Outline each blood parasite and name the species.
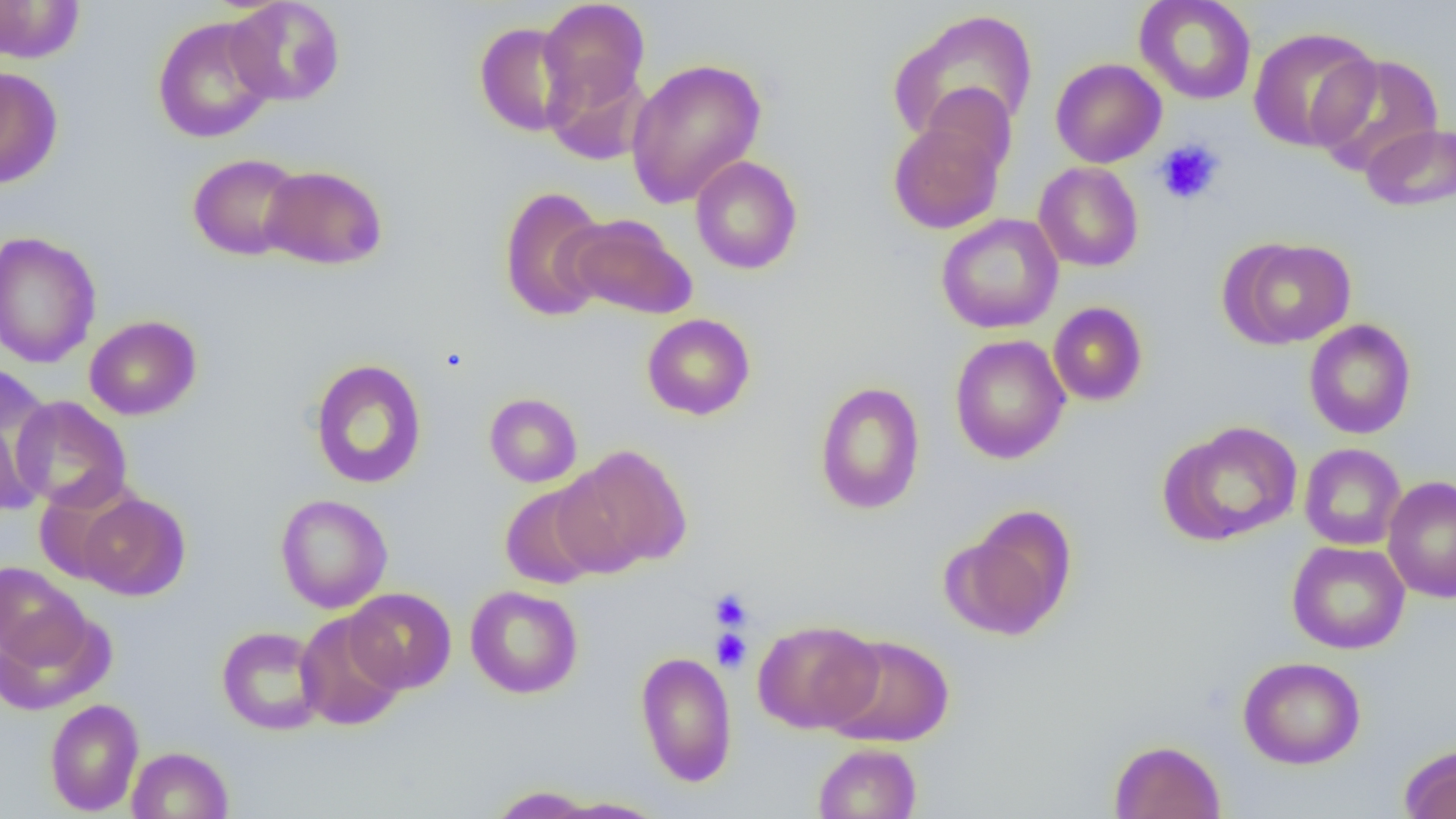
No blood parasites seen.

Approximate bounding boxes as named x1/y1/x2/y2 corners in pixels. Uninfected red blood cell locations: (x1=226, y1=0, x2=346, y2=106), (x1=1134, y1=0, x2=1257, y2=105), (x1=0, y1=1, x2=84, y2=63), (x1=538, y1=1, x2=650, y2=109), (x1=888, y1=8, x2=1038, y2=145), (x1=152, y1=15, x2=277, y2=144), (x1=474, y1=22, x2=579, y2=137), (x1=1248, y1=26, x2=1380, y2=152), (x1=1310, y1=52, x2=1445, y2=177), (x1=625, y1=58, x2=767, y2=208), (x1=1050, y1=58, x2=1166, y2=168), (x1=543, y1=59, x2=652, y2=166), (x1=0, y1=66, x2=63, y2=189), (x1=919, y1=83, x2=1018, y2=180), (x1=888, y1=119, x2=1005, y2=234), (x1=1361, y1=123, x2=1456, y2=211), (x1=187, y1=153, x2=305, y2=261), (x1=689, y1=155, x2=802, y2=275), (x1=1033, y1=161, x2=1144, y2=272), (x1=260, y1=164, x2=388, y2=270), (x1=498, y1=186, x2=612, y2=323), (x1=564, y1=213, x2=698, y2=320), (x1=936, y1=213, x2=1064, y2=334), (x1=0, y1=230, x2=102, y2=369), (x1=1221, y1=236, x2=1357, y2=349), (x1=1048, y1=302, x2=1148, y2=406), (x1=642, y1=313, x2=755, y2=420), (x1=84, y1=315, x2=201, y2=420), (x1=1303, y1=319, x2=1416, y2=439), (x1=950, y1=334, x2=1070, y2=464), (x1=309, y1=359, x2=428, y2=489), (x1=1, y1=376, x2=54, y2=512), (x1=813, y1=381, x2=926, y2=515), (x1=484, y1=393, x2=582, y2=487), (x1=10, y1=396, x2=132, y2=511), (x1=1159, y1=421, x2=1302, y2=546), (x1=1299, y1=443, x2=1406, y2=550), (x1=555, y1=444, x2=692, y2=575), (x1=1383, y1=475, x2=1456, y2=603), (x1=499, y1=484, x2=606, y2=590), (x1=77, y1=492, x2=190, y2=600), (x1=275, y1=494, x2=393, y2=614), (x1=944, y1=507, x2=1078, y2=640), (x1=1286, y1=540, x2=1410, y2=654), (x1=0, y1=563, x2=88, y2=668), (x1=465, y1=585, x2=583, y2=698), (x1=344, y1=587, x2=457, y2=694), (x1=0, y1=607, x2=114, y2=715), (x1=294, y1=611, x2=407, y2=731), (x1=752, y1=619, x2=882, y2=733), (x1=216, y1=625, x2=327, y2=736), (x1=823, y1=634, x2=956, y2=747), (x1=634, y1=650, x2=737, y2=787), (x1=1238, y1=655, x2=1366, y2=770), (x1=44, y1=698, x2=144, y2=816), (x1=1109, y1=739, x2=1226, y2=819), (x1=813, y1=742, x2=921, y2=819), (x1=1399, y1=744, x2=1456, y2=819), (x1=127, y1=746, x2=234, y2=818), (x1=487, y1=786, x2=600, y2=817), (x1=548, y1=797, x2=669, y2=818). Platelet locations: (x1=1155, y1=139, x2=1225, y2=206), (x1=709, y1=589, x2=753, y2=631), (x1=711, y1=629, x2=751, y2=672). Slide-level diagnosis: negative for blood parasites. Image is 1456×819 pixels. Captured at 1000x magnification. Thin blood film. One field of a larger specimen. Light microscopy.